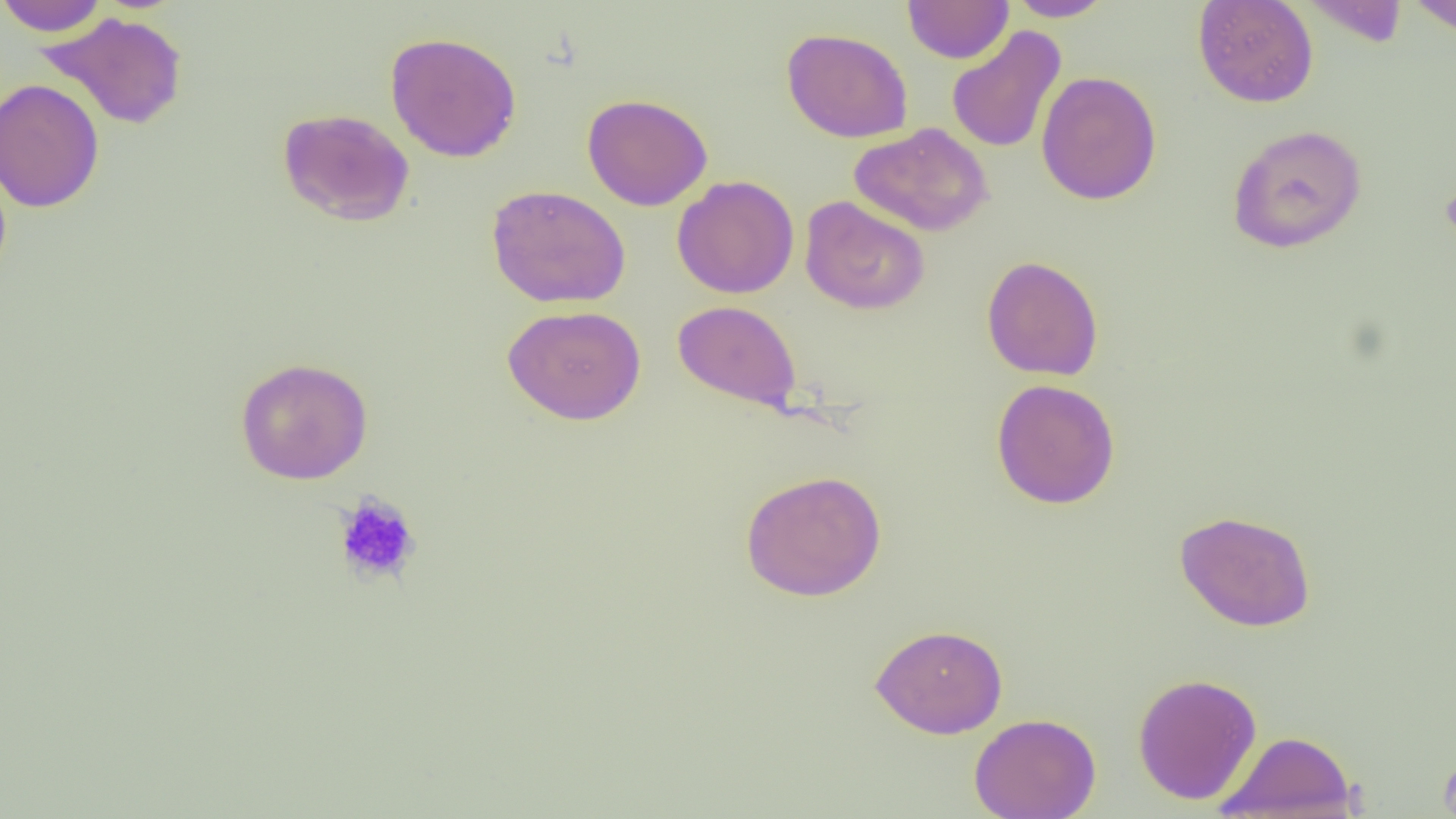
slide_level_diagnosis: no evidence of blood parasites
platelet_locations: 'approximate bounding boxes as (x1,y1)-(x2,y2) corner pairs in pixels: (1440,181)-(1456,247), (334,493)-(422,586)'
uninfected_red_blood_cell_locations: 'approximate bounding boxes as (x1,y1)-(x2,y2) corner pairs in pixels: (0,0)-(110,36), (902,0)-(1014,64), (1004,0)-(1116,21), (1193,0)-(1319,108), (1298,1)-(1412,47), (1403,1)-(1456,35), (38,11)-(188,130), (946,25)-(1066,154), (781,28)-(914,143), (385,31)-(522,162), (1036,71)-(1162,205), (0,78)-(104,213), (582,93)-(713,211), (277,108)-(414,226), (850,123)-(994,237), (1226,124)-(1367,254), (671,175)-(800,299), (486,184)-(631,308), (800,196)-(930,315), (981,255)-(1104,381), (673,300)-(801,410), (502,305)-(646,425), (234,357)-(374,485), (991,378)-(1121,510), (740,469)-(887,602), (1174,509)-(1316,632), (870,623)-(1008,739), (1132,672)-(1262,804), (969,713)-(1101,819), (1217,730)-(1358,818)'
field_of_view: one of a larger specimen
image_size: 1456×819 pixels
magnification: 1000x
preparation: thin blood smear
modality: optical microscopy